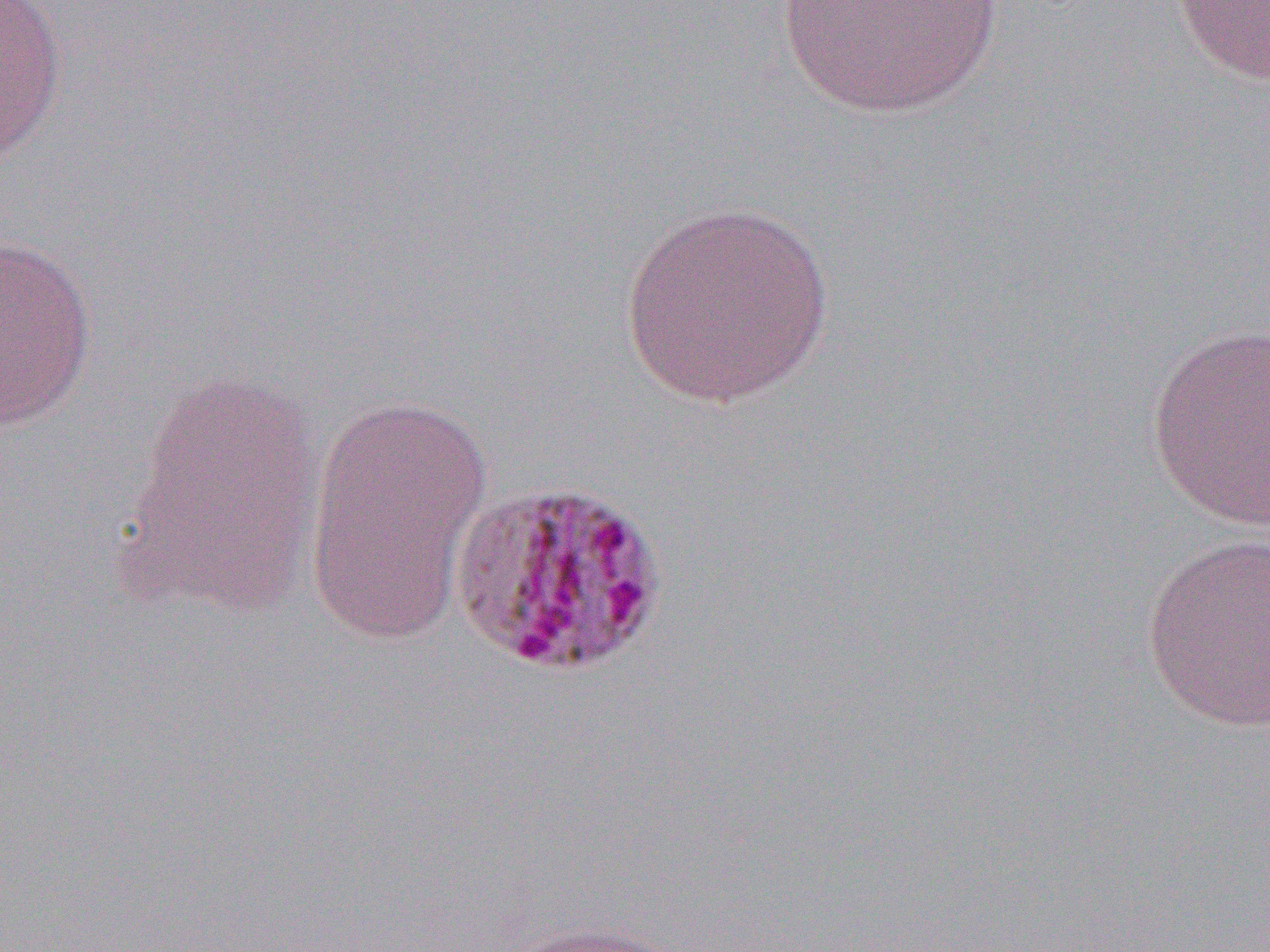
slide_level_diagnosis: Plasmodium malariae
preparation: thin blood film
image_size: 1270×952 pixels
magnification: 1000x
uninfected_red_blood_cell_locations: 'approximate bounding boxes as (x1,y1)-(x2,y2) corner pairs in pixels: (774,0)-(1006,119), (1171,0)-(1270,85), (0,1)-(68,167), (617,201)-(834,408), (0,233)-(98,431), (1145,322)-(1270,531), (118,368)-(326,617), (303,394)-(493,646), (1140,532)-(1269,733), (494,920)-(691,952)'
modality: light microscopy
field_of_view: one of a larger specimen